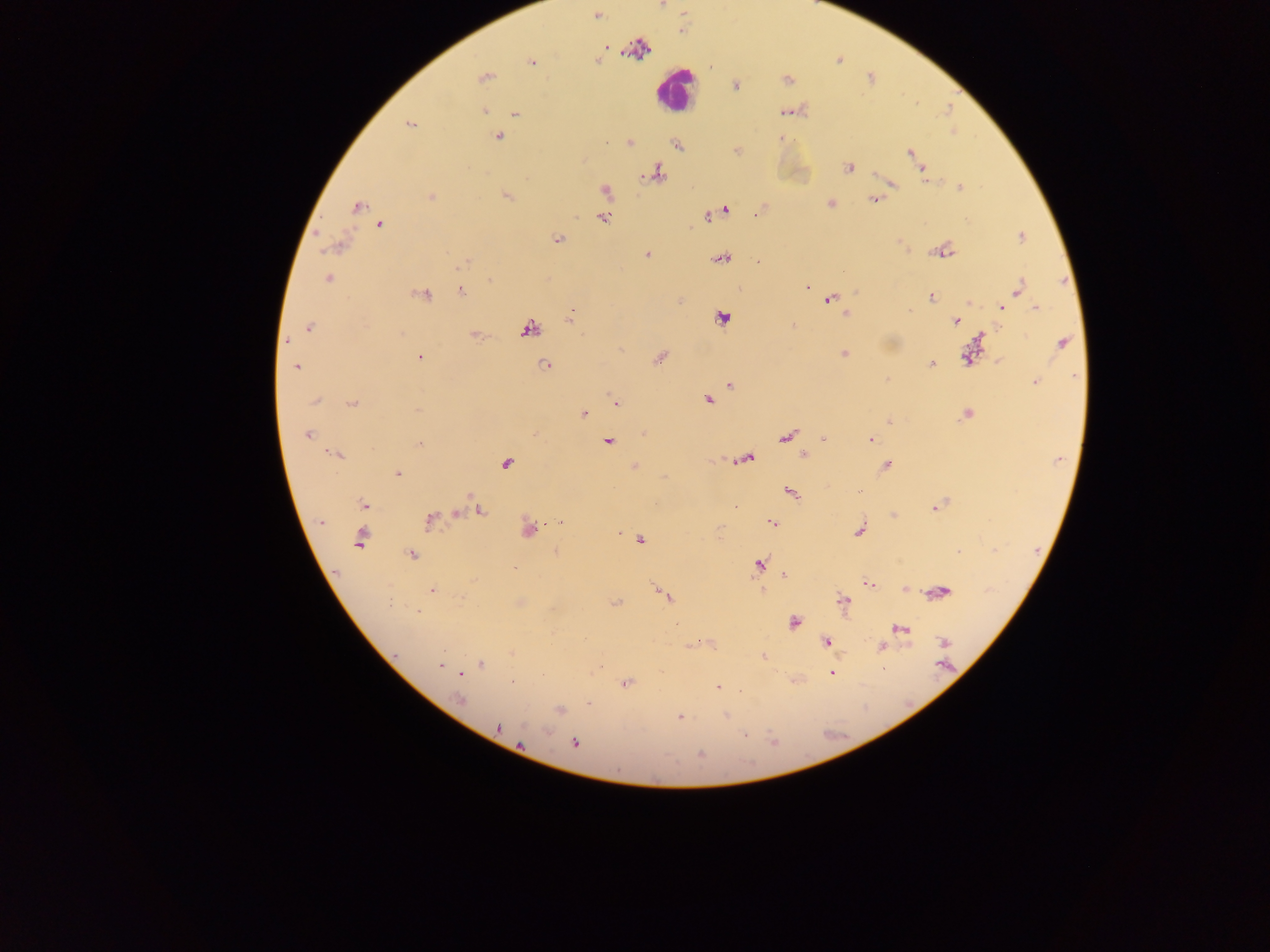
Approximate centers as x y in pixels. Plasmodium parasite locations: 597 15; 606 47; 598 61; 532 62; 483 78; 788 80; 735 85; 484 111; 515 114; 409 125; 498 136; 630 142; 678 145; 910 153; 848 168; 923 171; 656 173; 891 184; 960 187; 606 191; 506 196; 430 197; 873 199; 830 203; 357 207; 725 211; 710 216; 601 217; 379 225; 1021 237; 557 239; 337 246; 943 252; 647 254; 722 259; 758 262; 464 263; 328 278; 490 280; 1018 287; 808 288; 462 292; 425 295; 930 297; 830 300; 970 302; 1002 308; 1036 308; 910 310; 571 313; 845 313; 723 318; 956 321; 793 326; 308 328; 529 328; 287 341; 1062 343; 844 353; 419 357; 967 357; 660 358; 931 364; 296 366; 546 366; 887 379; 1034 382; 730 385; 707 400; 315 401; 616 402; 352 404; 417 410; 583 414; 966 414; 890 422; 307 435; 786 437; 822 437; 871 439; 608 442; 420 444; 334 454; 804 455; 748 457; 507 463; 886 465; 634 466; 398 473; 859 492; 791 493; 363 504; 936 507; 480 510; 456 514; 429 519; 320 522; 558 523; 772 523; 529 530; 859 530; 361 539; 641 541; 958 552; 412 555; 759 564; 515 569; 784 576; 868 585; 906 589; 431 590; 762 591; 942 592; 665 595; 844 601; 615 603; 419 612; 794 623; 900 628; 944 642; 826 643; 882 646; 396 653; 763 656; 481 664; 440 665; 944 666; 832 673; 461 674; 512 682; 626 683; 718 688; 740 691; 458 700; 588 704; 560 710; 726 716; 680 717; 498 727; 745 736; 574 743; 701 754. Leukocyte locations: 672 91. Sample from Ghana. Single field of view. Image is 1270×952 pixels. Thick blood smear. Photographed through a microscope with a mobile-phone camera.